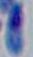

Summary:
  - Identification: Toxoplasma gondii
  - Modality: micrograph
  - Magnification: 1000x